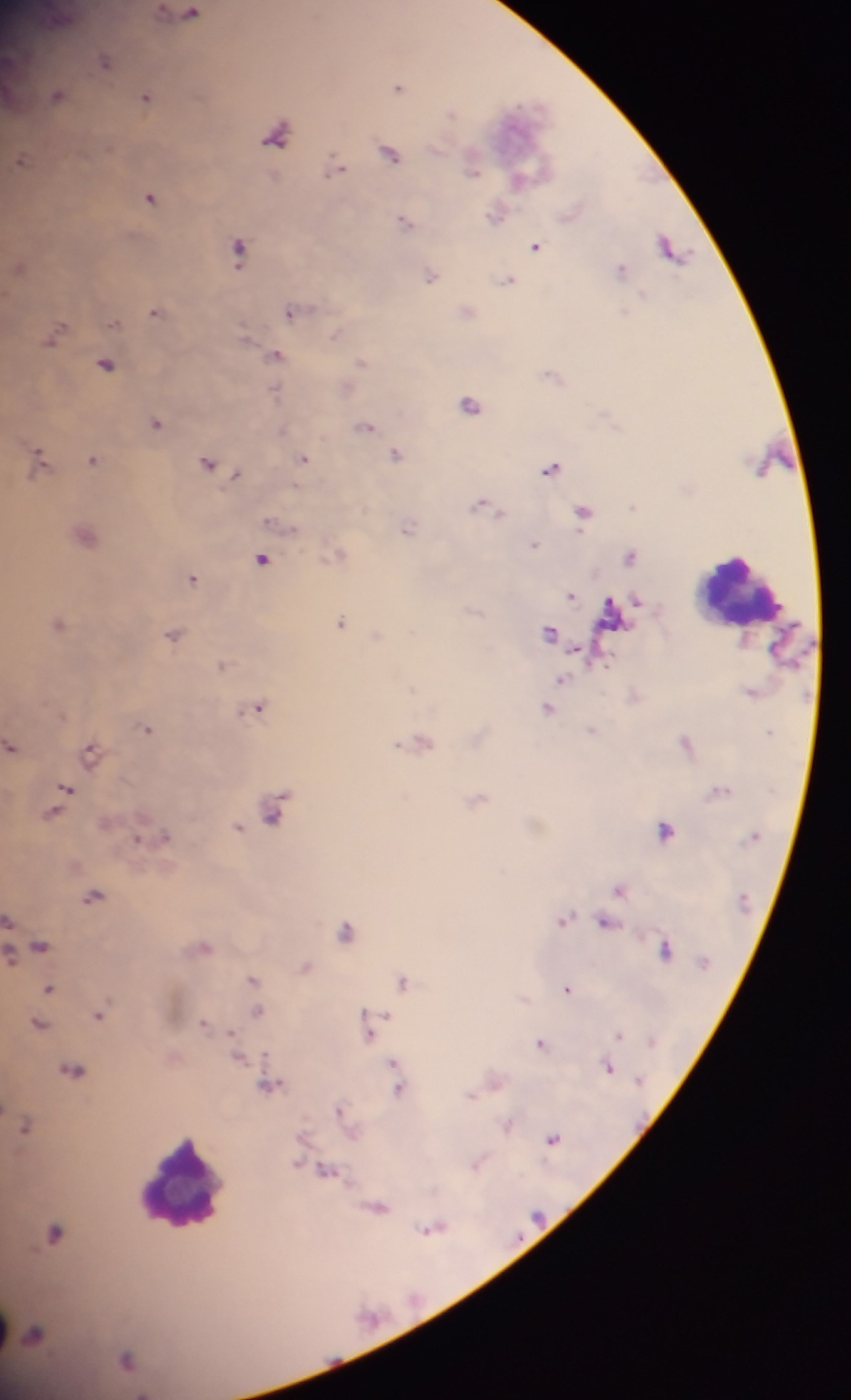 Approximate centers as {x, y} in pixels. Malaria parasite locations: {190, 13}, {104, 60}, {398, 86}, {55, 95}, {145, 97}, {451, 112}, {388, 153}, {21, 160}, {334, 166}, {471, 170}, {523, 175}, {149, 197}, {495, 215}, {403, 221}, {535, 246}, {237, 249}, {670, 249}, {618, 270}, {430, 276}, {506, 280}, {154, 311}, {290, 311}, {113, 324}, {54, 334}, {275, 355}, {361, 362}, {105, 364}, {274, 393}, {469, 404}, {155, 423}, {364, 426}, {396, 454}, {302, 458}, {37, 459}, {92, 459}, {207, 462}, {550, 468}, {235, 475}, {483, 506}, {583, 513}, {406, 529}, {533, 545}, {630, 557}, {261, 559}, {192, 578}, {571, 595}, {339, 622}, {57, 624}, {548, 632}, {172, 634}, {222, 665}, {557, 682}, {256, 706}, {547, 709}, {145, 728}, {592, 731}, {686, 742}, {10, 746}, {90, 752}, {64, 789}, {718, 791}, {274, 811}, {53, 813}, {237, 828}, {664, 830}, {163, 836}, {137, 839}, {618, 888}, {91, 896}, {564, 919}, {7, 921}, {604, 921}, {345, 930}, {38, 945}, {203, 947}, {663, 949}, {304, 967}, {251, 978}, {402, 981}, {48, 988}, {565, 988}, {257, 1012}, {99, 1014}, {204, 1023}, {38, 1024}, {368, 1026}, {618, 1036}, {540, 1044}, {238, 1056}, {392, 1066}, {607, 1067}, {72, 1070}, {268, 1086}, {398, 1086}, {471, 1094}, {339, 1109}, {25, 1126}, {506, 1126}, {552, 1137}, {476, 1163}, {324, 1169}, {376, 1206}, {430, 1228}, {53, 1233}, {34, 1333}, {125, 1359}. Leukocyte locations: {739, 595}, {182, 1183}. Image is 851×1400 pixels. Single field of view. Photographed through a microscope with a mobile-phone camera. Sample from Ghana. Thick blood smear.